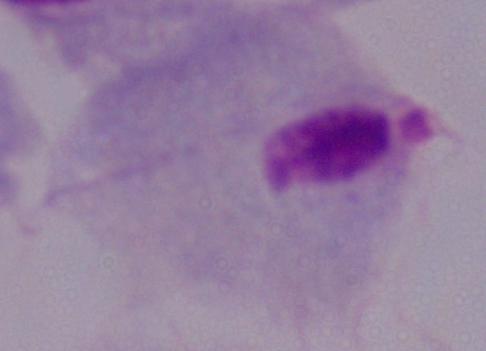

modality = micrograph
magnification = 1000x
identification = trichomonad